Point out each malaria parasite.
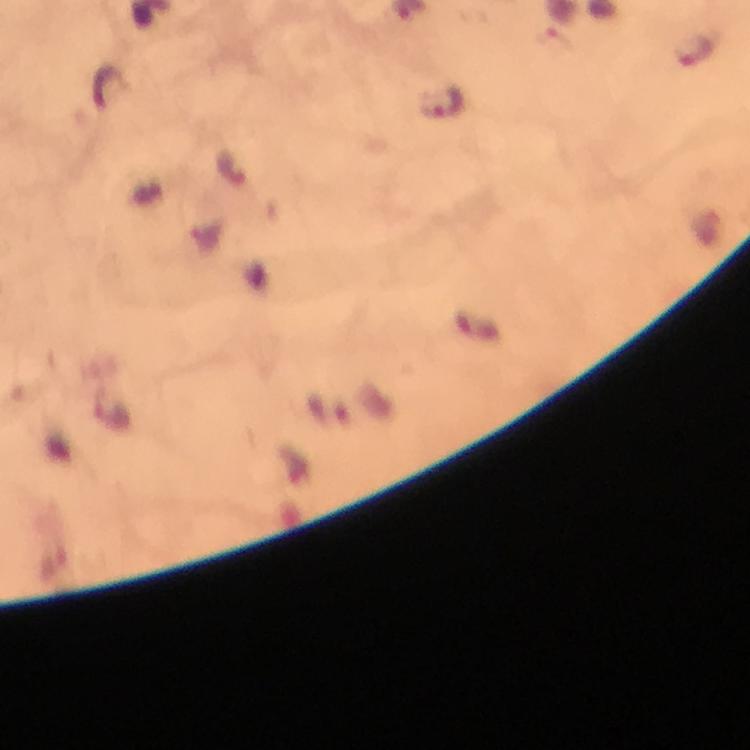

Approximate centers as {x, y} in pixels.
Malaria parasites: {695, 51}, {442, 103}, {232, 169}.

Summary:
  - Context: from a malaria diagnostic workup
  - Immersion oil: applied
  - Stain: Giemsa
  - Capture: smartphone camera through the microscope
  - Preparation: thick blood smear
  - Cropped from: a single field of view
  - Image size: 750×750 pixels
  - Magnification: 100x